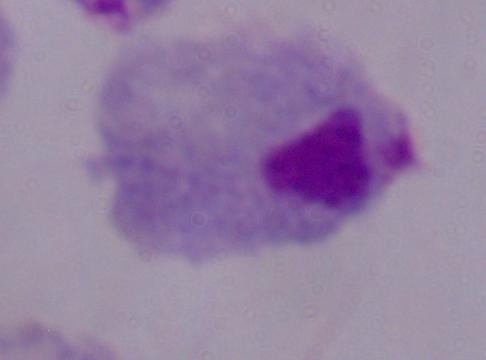
identification: trichomonad
modality: photomicrograph
magnification: 1000x